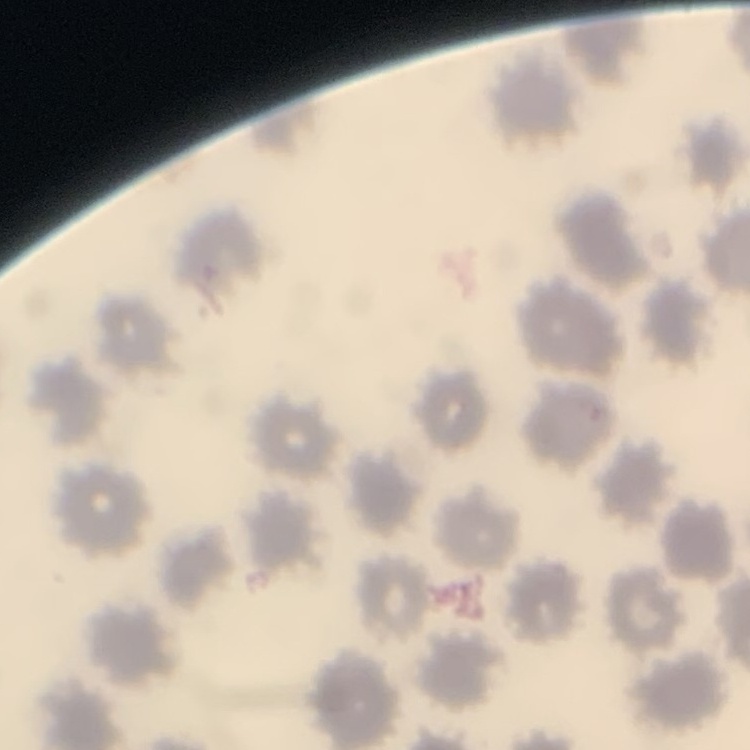
red blood cell morphology = no rouleaux formation
image type = square crop of a larger photomicrograph
preparation = thin blood smear
stain = Field's or Giemsa